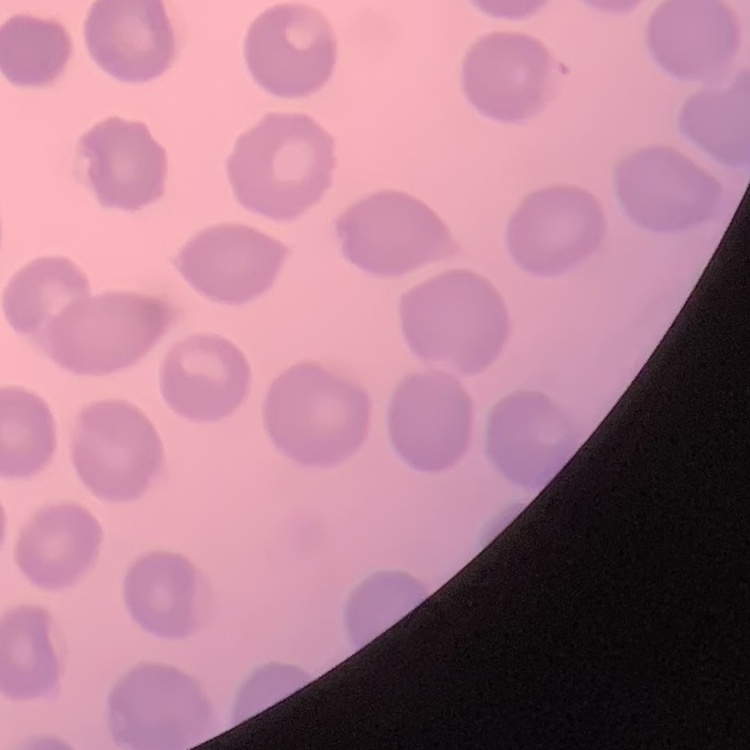

Summary:
  - Erythrocyte morphology: no rouleaux formation
  - Image type: one tile cut from a larger photomicrograph
  - Preparation: thin peripheral smear
  - Stain: Field's or Giemsa